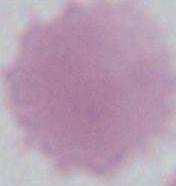
1000x magnification. Photomicrograph. An erythrocyte is seen.